State which cell type is depicted.
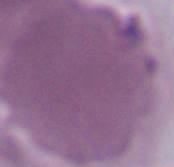

This is an erythrocyte.

Summary:
  - Modality: micrograph
  - Magnification: 1000x